Locate every Plasmodium parasite.
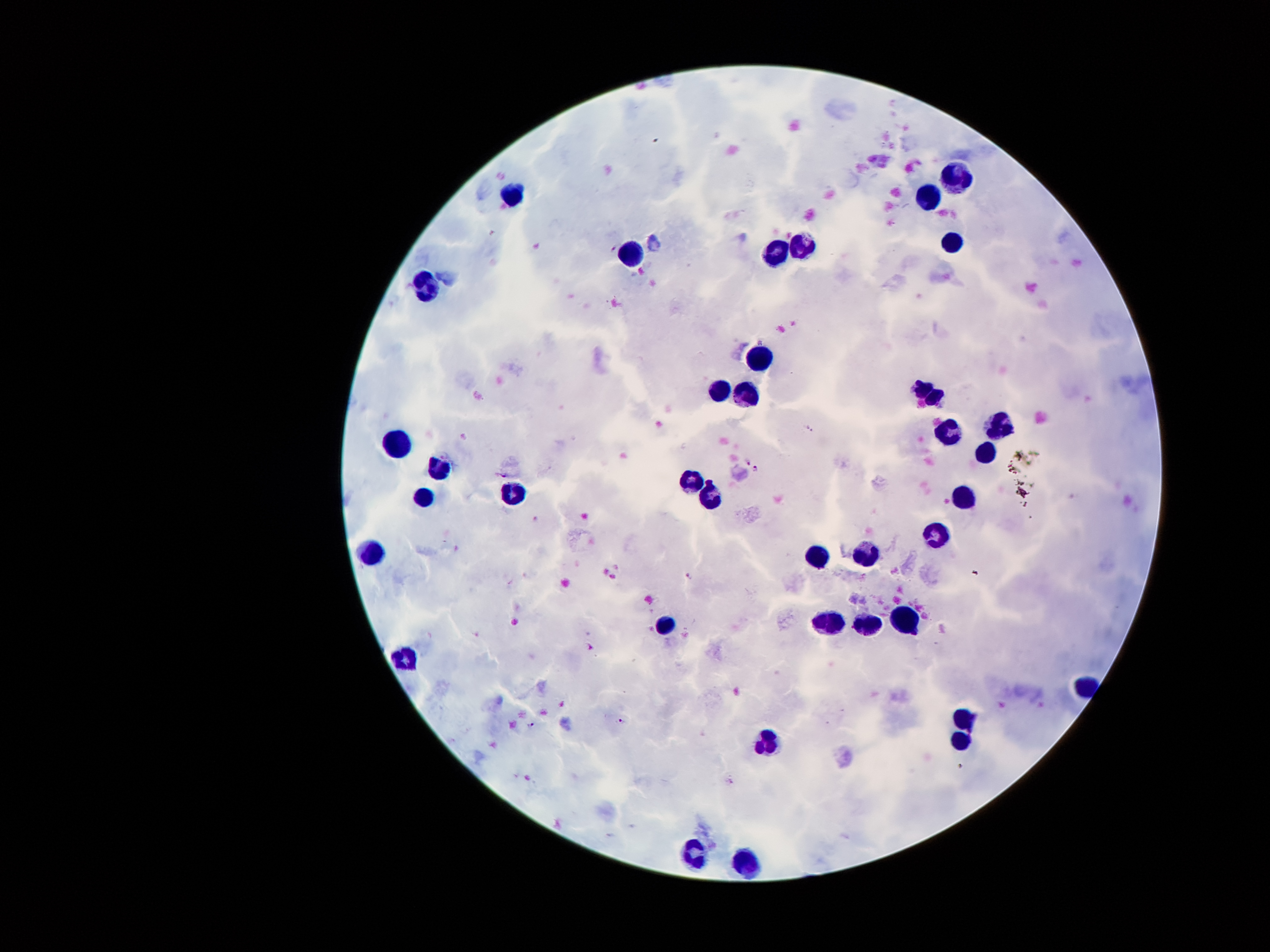

Approximate centers as [x, y] in pixels.
Plasmodium parasites: [612, 248], [747, 460], [757, 468], [503, 474], [688, 576], [589, 646], [620, 719], [530, 724].

Leukocyte locations: [955, 177], [514, 195], [926, 199], [802, 240], [949, 240], [628, 252], [769, 252], [426, 287], [759, 360], [715, 391], [928, 392], [744, 396], [994, 426], [949, 433], [396, 446], [986, 453], [437, 471], [689, 481], [513, 491], [963, 494], [711, 498], [421, 499], [937, 532], [377, 550], [867, 553], [818, 556], [902, 618], [830, 623], [866, 625], [666, 627], [408, 654], [965, 719], [765, 745], [961, 745], [694, 857], [749, 861]. 100x magnification. One field from this slide. Giemsa stain. Photographed through the microscope eyepiece with a smartphone camera. Thick blood film. Image is 1270×952 pixels. Patient malaria status: infected with Plasmodium falciparum.